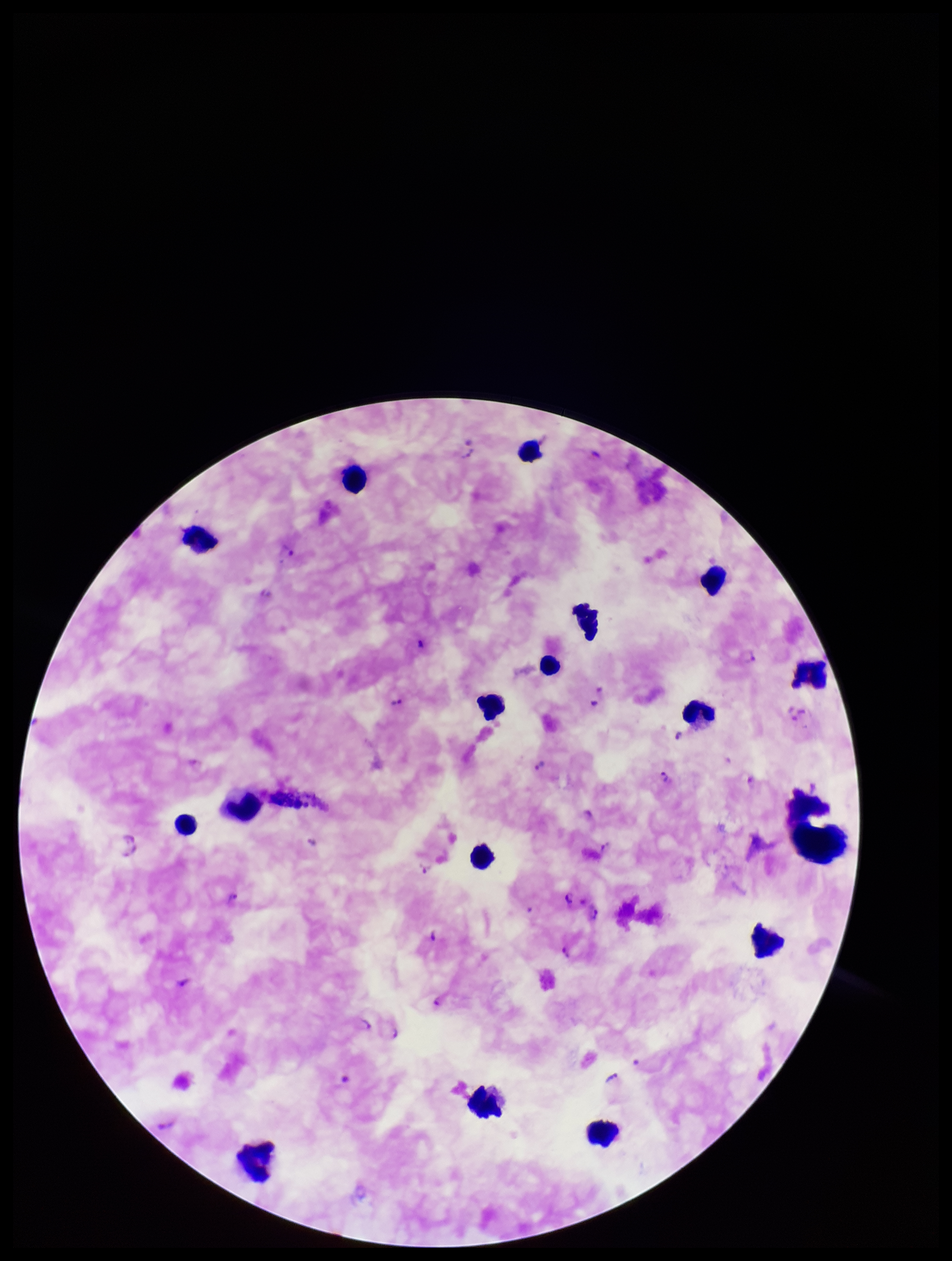

Summary:
  - Capture: smartphone photograph through the microscope eyepiece
  - Patient malaria status: infected
  - Stain: Giemsa
  - Field of view: single
  - Plasmodium parasites: seen
  - Image size: 952×1261 pixels
  - Parasite count: 17
  - Species reported for this patient: Plasmodium falciparum
  - Leukocyte count: 15
  - Preparation: thick smear